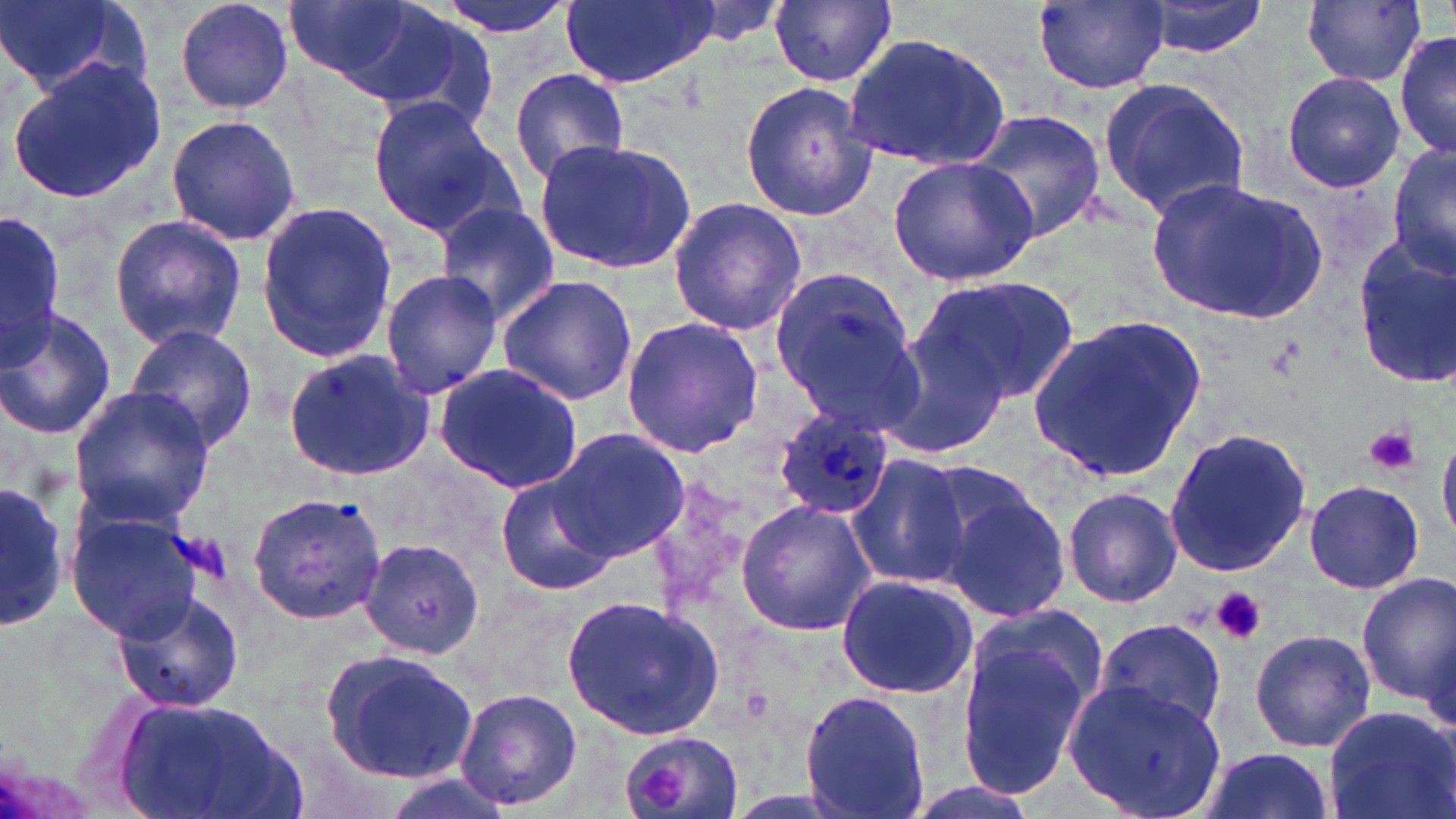
Approximate bounding boxes as [x1, y1, x2, y2] in pixels. Platelet locations: [1365, 424, 1418, 476], [1211, 587, 1268, 644], [637, 765, 686, 809]. Uninfected red blood cell locations: [0, 0, 127, 92], [173, 0, 295, 115], [280, 0, 424, 84], [429, 0, 576, 40], [562, 0, 718, 90], [769, 0, 897, 87], [1032, 0, 1169, 92], [310, 1, 491, 115], [1142, 1, 1270, 56], [1304, 2, 1427, 88], [1394, 24, 1454, 162], [841, 28, 1014, 172], [7, 57, 166, 206], [509, 68, 632, 189], [1281, 71, 1405, 194], [1096, 77, 1251, 216], [738, 81, 880, 221], [364, 93, 516, 240], [970, 109, 1106, 246], [165, 114, 301, 247], [532, 137, 696, 274], [1388, 137, 1456, 285], [886, 156, 1039, 285], [1145, 179, 1323, 323], [666, 196, 810, 336], [254, 199, 397, 364], [435, 203, 559, 326], [0, 208, 65, 370], [108, 212, 249, 351], [1350, 238, 1456, 386], [764, 261, 925, 435], [380, 270, 505, 397], [496, 273, 638, 405], [920, 276, 1078, 401], [0, 309, 117, 440], [1027, 315, 1208, 487], [621, 316, 765, 457], [870, 321, 1016, 464], [123, 324, 260, 454], [283, 347, 435, 482], [434, 363, 585, 495], [67, 384, 217, 527], [1163, 427, 1314, 580], [552, 428, 692, 562], [1438, 440, 1456, 543], [845, 454, 969, 588], [927, 469, 1074, 624], [493, 474, 617, 597], [0, 480, 67, 635], [1302, 480, 1421, 594], [1061, 486, 1181, 608], [248, 490, 387, 625], [735, 498, 877, 637], [65, 508, 206, 644], [359, 535, 486, 657], [835, 573, 981, 700], [1356, 573, 1455, 709], [110, 589, 246, 714], [561, 593, 723, 743], [956, 607, 1109, 796], [1094, 618, 1230, 736], [1249, 629, 1376, 753], [322, 647, 479, 783], [1065, 679, 1228, 819], [453, 688, 582, 812], [801, 688, 929, 819], [108, 692, 307, 819], [1320, 705, 1454, 819], [616, 730, 746, 819], [1196, 745, 1336, 819], [896, 779, 1044, 819]. Plasmodium ovale-infected red blood cell locations: [771, 410, 897, 522]. Slide-level diagnosis: Plasmodium ovale. Captured at 1000x magnification. Optical microscopy. Thin blood film. May-Grünwald-Giemsa stain. Image is 1456×819 pixels. One field of a larger specimen.